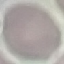

Result: negative for malaria parasites. Giemsa-stained preparation. Automatically extracted cell patch, resized to 64 × 64 pixels. Thin blood film. Acquired by smartphone through the microscope eyepiece.